Locate and identify every blood parasite.
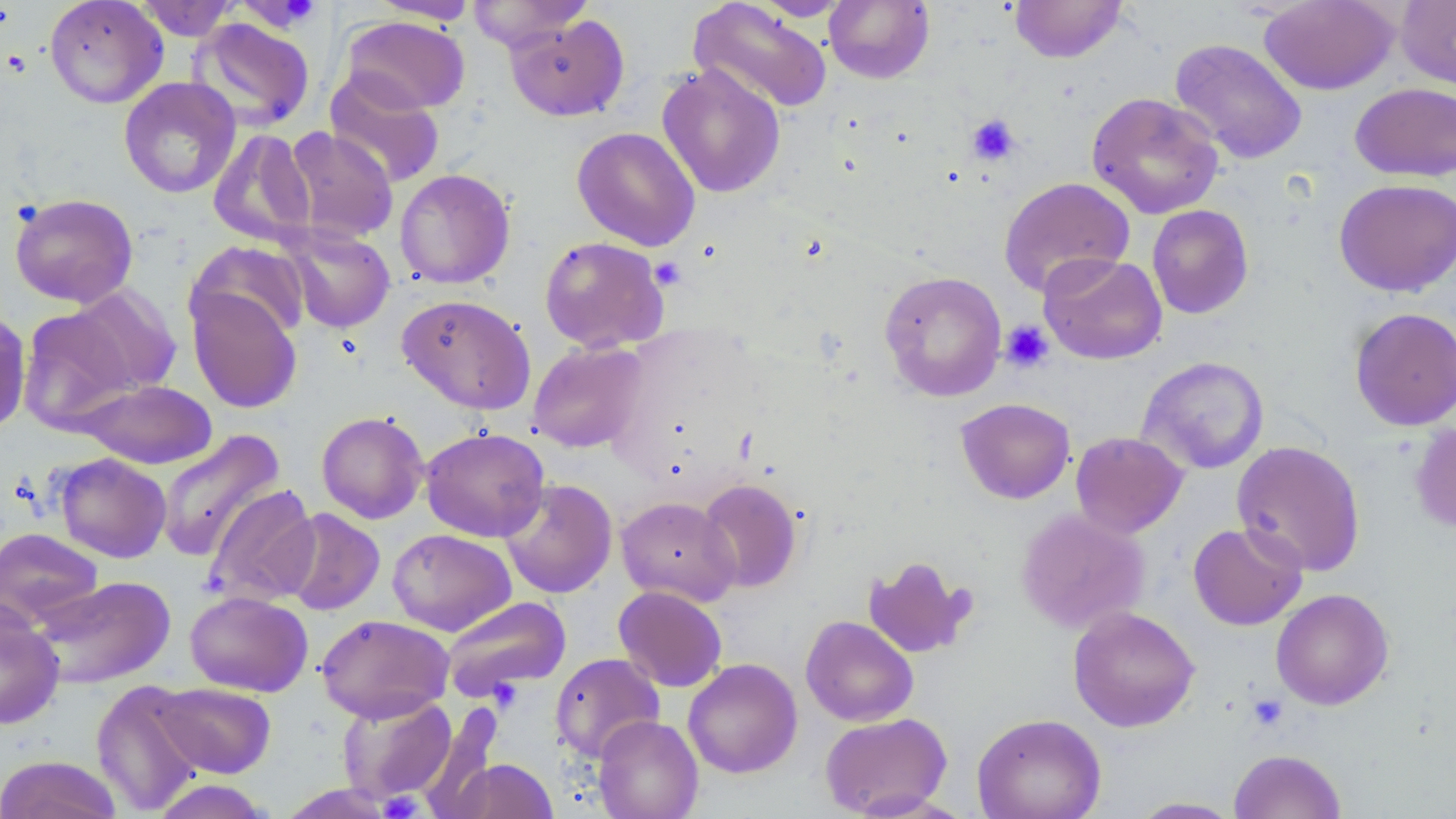
No blood parasites observed.

Approximate bounding boxes as [x1, y1, x2, y2] in pixels. Uninfected red blood cell locations: [44, 0, 168, 108], [135, 0, 239, 41], [233, 0, 324, 32], [368, 0, 480, 24], [467, 0, 593, 53], [751, 0, 853, 21], [824, 0, 935, 84], [1010, 0, 1127, 63], [1258, 0, 1398, 95], [1396, 0, 1456, 91], [688, 1, 833, 115], [506, 14, 629, 122], [341, 16, 470, 114], [188, 17, 316, 132], [1169, 39, 1308, 164], [656, 62, 786, 199], [324, 71, 446, 189], [118, 77, 241, 199], [1350, 82, 1456, 182], [1087, 92, 1224, 220], [571, 126, 700, 251], [284, 127, 399, 243], [207, 129, 317, 247], [394, 168, 515, 289], [998, 176, 1135, 298], [1333, 178, 1456, 297], [10, 192, 139, 308], [1146, 204, 1254, 319], [280, 224, 395, 334], [539, 235, 670, 354], [186, 240, 311, 341], [1039, 252, 1168, 365], [878, 270, 1007, 402], [66, 285, 182, 395], [187, 287, 303, 414], [397, 294, 536, 415], [1349, 306, 1456, 431], [18, 307, 138, 432], [0, 311, 31, 437], [528, 341, 649, 453], [1137, 356, 1270, 474], [76, 379, 216, 469], [955, 397, 1075, 504], [316, 411, 429, 524], [1410, 421, 1456, 535], [420, 427, 550, 542], [156, 429, 285, 562], [1071, 431, 1188, 538], [1231, 440, 1366, 577], [54, 453, 171, 563], [499, 478, 617, 598], [696, 478, 803, 593], [204, 484, 321, 607], [616, 496, 740, 606], [280, 508, 385, 616], [1016, 508, 1150, 634], [1188, 522, 1307, 630], [0, 527, 103, 629], [387, 528, 516, 636], [863, 555, 976, 658], [31, 576, 176, 689], [613, 586, 728, 692], [1270, 588, 1394, 710], [185, 590, 313, 697], [440, 596, 572, 700], [0, 605, 64, 729], [1068, 606, 1200, 732], [316, 614, 454, 723], [800, 615, 918, 726], [550, 653, 665, 763], [683, 658, 803, 779], [91, 680, 206, 815], [154, 682, 276, 778], [337, 693, 457, 804], [418, 701, 504, 819], [819, 712, 953, 817], [972, 713, 1107, 819], [592, 715, 704, 819], [1229, 749, 1346, 819], [0, 755, 123, 818], [451, 758, 558, 818], [147, 779, 276, 819], [273, 784, 400, 818], [1130, 797, 1244, 818]. Platelet locations: [238, 0, 321, 31], [966, 114, 1020, 165], [649, 256, 686, 291], [1000, 320, 1054, 373], [1248, 694, 1288, 732], [378, 791, 425, 818]. Slide-level diagnosis: negative for blood parasites. May-Grünwald-Giemsa stain. Optical microscopy. Thin blood film. Image is 1456×819 pixels. 1000x magnification. Single field of view.